Comment on the morphology of the red blood cells.
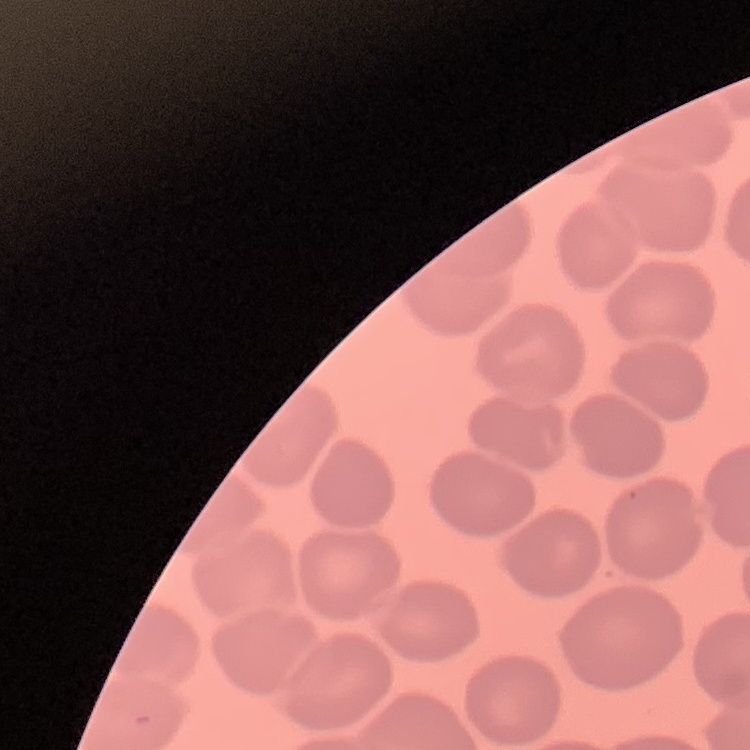
No rouleaux formation.

stain: Field's or Giemsa
image_type: square crop of a larger photomicrograph
preparation: thin blood smear